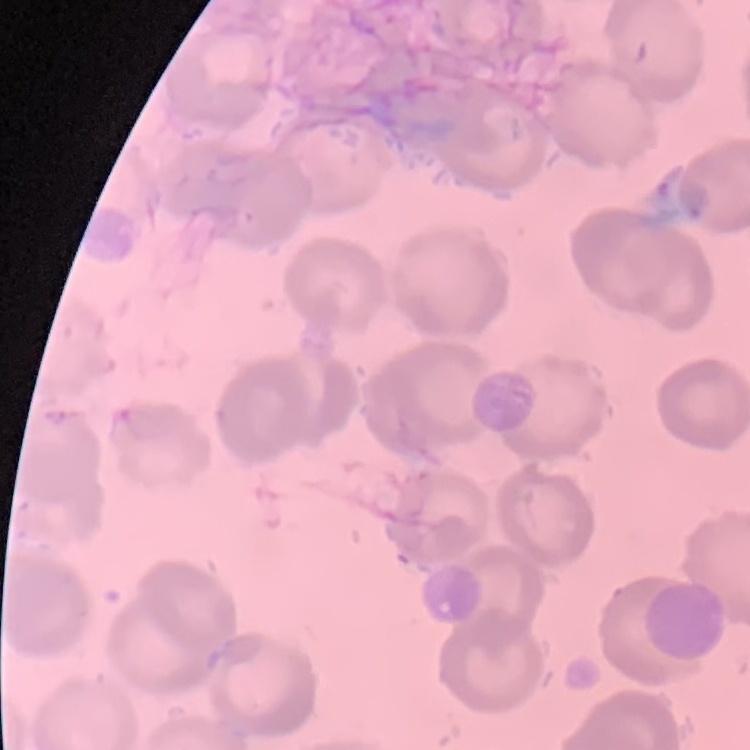

The erythrocytes exhibit no rouleaux formation. Thin peripheral smear. Square crop of a larger photomicrograph. Stained with either Field's or Giemsa.